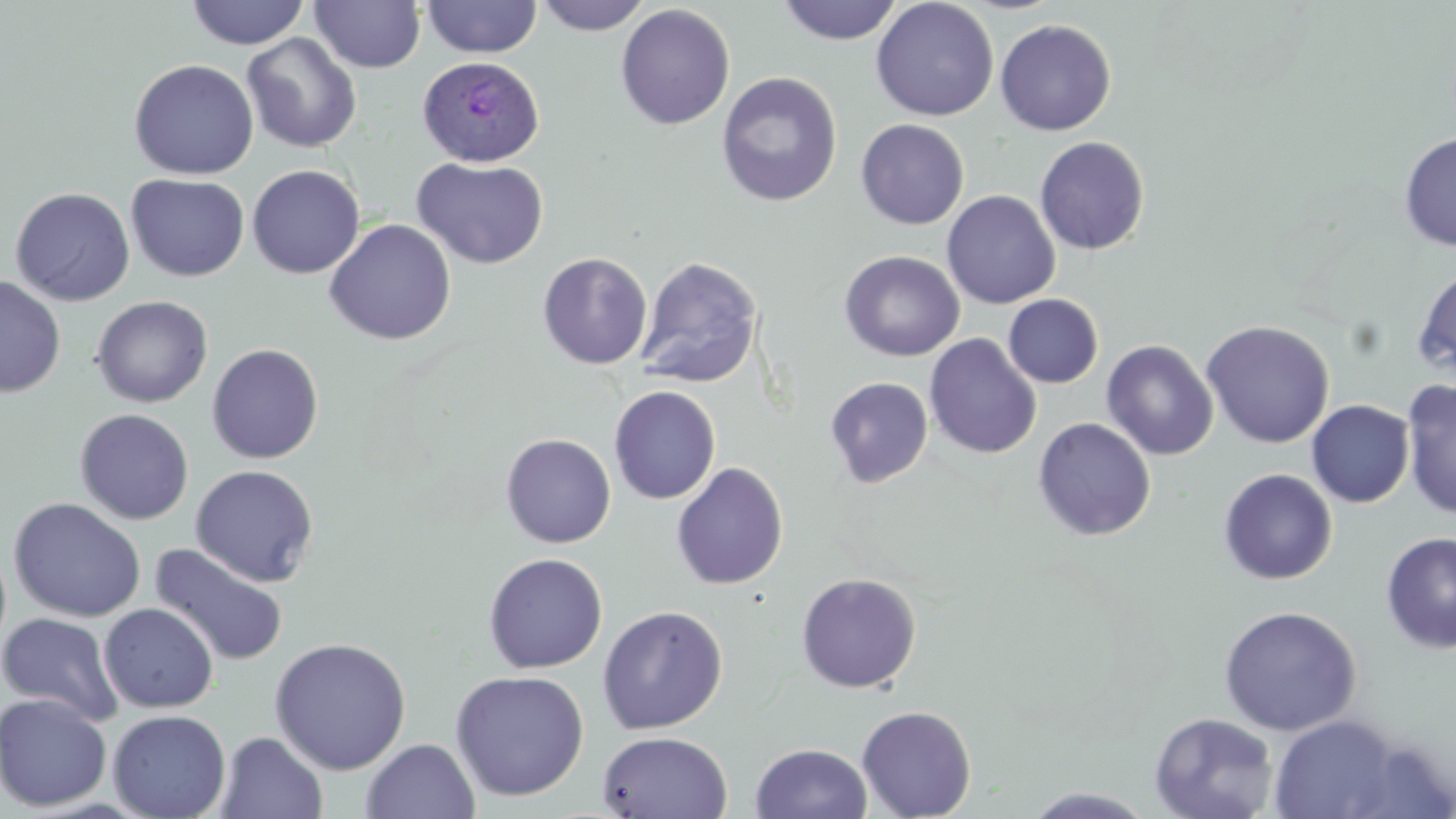
Approximate bounding boxes as [x1, y1, x2, y2] in pixels. Plasmodium ovale-infected red blood cell locations: [418, 54, 544, 168]. Uninfected red blood cell locations: [421, 0, 542, 59], [533, 0, 653, 35], [777, 0, 903, 45], [871, 0, 999, 121], [185, 1, 311, 49], [310, 1, 426, 74], [615, 4, 736, 130], [995, 18, 1116, 136], [242, 33, 362, 154], [129, 59, 259, 179], [716, 72, 842, 208], [856, 118, 969, 229], [1399, 132, 1456, 251], [1034, 136, 1150, 255], [411, 156, 549, 269], [247, 164, 365, 279], [126, 174, 250, 281], [11, 186, 135, 306], [941, 190, 1060, 309], [324, 219, 456, 345], [839, 250, 965, 362], [537, 252, 652, 369], [636, 255, 763, 388], [1413, 264, 1456, 381], [0, 275, 66, 398], [1003, 294, 1103, 388], [91, 295, 213, 408], [1202, 320, 1335, 448], [924, 333, 1042, 459], [1101, 340, 1218, 460], [206, 343, 324, 463], [824, 377, 933, 488], [1401, 379, 1456, 520], [609, 385, 721, 504], [1307, 400, 1414, 507], [75, 408, 194, 524], [1033, 417, 1156, 541], [500, 433, 616, 548], [671, 462, 789, 590], [190, 464, 319, 587], [1218, 468, 1338, 584], [8, 497, 146, 622], [1380, 531, 1456, 654], [149, 543, 290, 668], [483, 552, 608, 673], [795, 572, 921, 692], [98, 603, 219, 713], [597, 605, 728, 734], [1218, 605, 1363, 736], [0, 612, 125, 726], [269, 636, 412, 775], [450, 669, 589, 801], [0, 693, 112, 812], [856, 705, 977, 818], [108, 709, 231, 818], [1149, 712, 1279, 819], [1268, 714, 1402, 818], [597, 730, 733, 817], [215, 731, 329, 819], [361, 737, 481, 819], [751, 742, 873, 819], [1019, 787, 1159, 818]. Slide-level diagnosis: Plasmodium ovale. May-Grünwald-Giemsa stain. Single field of view. Captured at 1000x magnification. Image is 1456×819 pixels. Optical microscopy. Thin blood smear.